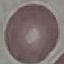

result = no malaria parasites detected
stain = Giemsa
image type = cell patch, automatically extracted from a larger field of view and resized to 64 × 64 pixels
capture = smartphone through the microscope eyepiece
preparation = thin smear